Locate every blood parasite and identify its species.
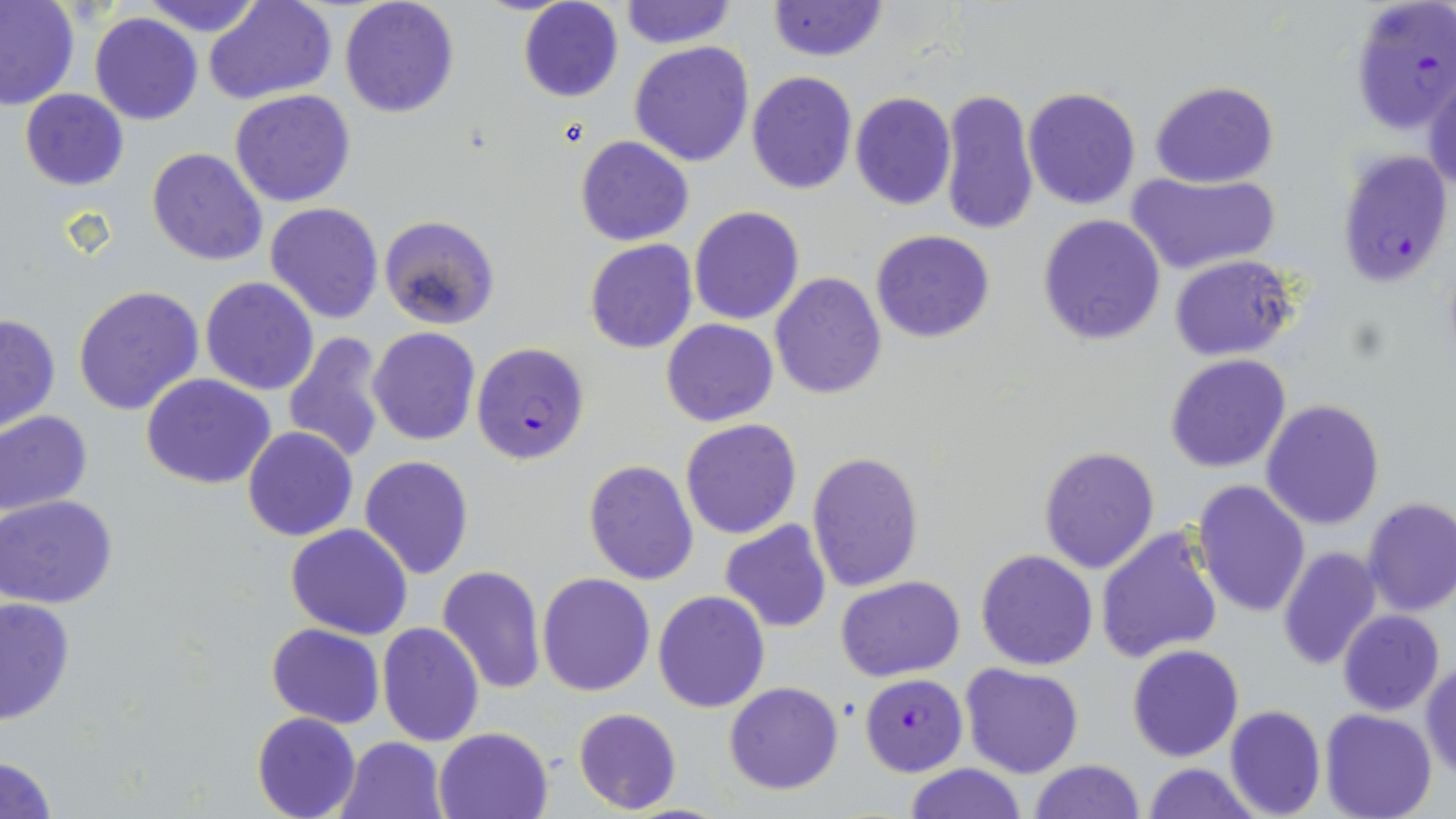
Approximate bounding boxes as [x1, y1, x2, y2] in pixels.
Plasmodium falciparum-infected red blood cells: [1348, 0, 1456, 140], [1335, 150, 1455, 287], [471, 342, 590, 465], [860, 673, 967, 775].
No Plasmodium ovale, Plasmodium malariae, Plasmodium vivax, Babesia divergens, or Trypanosoma brucei observed.

{
  "slide_level_diagnosis": "Plasmodium falciparum",
  "modality": "optical microscopy",
  "preparation": "thin blood smear",
  "uninfected_red_blood_cell_locations": "approximate bounding boxes as [x1, y1, x2, y2] in pixels: [0, 0, 80, 110], [140, 0, 265, 37], [338, 0, 459, 119], [618, 0, 736, 50], [205, 1, 335, 105], [767, 1, 888, 63], [517, 2, 623, 103], [90, 11, 203, 125], [630, 41, 755, 167], [747, 70, 858, 195], [1425, 71, 1456, 198], [1150, 81, 1279, 186], [1022, 86, 1141, 210], [20, 89, 128, 190], [230, 89, 356, 208], [940, 89, 1038, 236], [850, 92, 955, 211], [575, 135, 693, 246], [147, 147, 268, 265], [1126, 171, 1282, 274], [265, 202, 385, 324], [689, 206, 804, 325], [378, 214, 502, 331], [1038, 214, 1166, 345], [584, 222, 801, 340], [870, 229, 995, 343], [584, 239, 698, 355], [1169, 255, 1296, 360], [771, 272, 887, 399], [199, 275, 320, 396], [74, 284, 205, 415], [0, 313, 60, 432], [662, 319, 778, 426], [368, 327, 481, 446], [282, 331, 390, 466], [1166, 355, 1292, 473], [140, 374, 278, 491], [1261, 398, 1385, 531], [0, 410, 93, 520], [679, 418, 803, 539], [242, 427, 358, 543], [1039, 446, 1160, 574], [807, 451, 925, 593], [358, 456, 475, 579], [583, 460, 699, 584], [1192, 479, 1310, 618], [1, 495, 117, 608], [1362, 498, 1456, 617], [719, 521, 832, 634], [286, 523, 413, 638], [1094, 526, 1225, 666], [1277, 546, 1383, 671], [976, 549, 1098, 671], [437, 565, 546, 693], [537, 572, 655, 696], [836, 575, 965, 681], [653, 590, 771, 712], [0, 596, 76, 725], [1336, 610, 1445, 717], [377, 622, 484, 748], [265, 624, 385, 728], [1127, 644, 1244, 761], [1421, 662, 1455, 780], [961, 664, 1083, 778], [724, 681, 843, 795], [1225, 704, 1326, 818], [572, 708, 682, 813], [1321, 709, 1436, 819], [251, 712, 360, 819], [434, 727, 552, 819], [337, 736, 449, 819], [0, 755, 57, 817], [1029, 759, 1146, 818], [903, 763, 1027, 819], [1143, 764, 1260, 819]",
  "image_size": "1456×819 pixels",
  "stain": "May-Grünwald-Giemsa",
  "field_of_view": "one of a larger specimen",
  "magnification": "1000x"
}